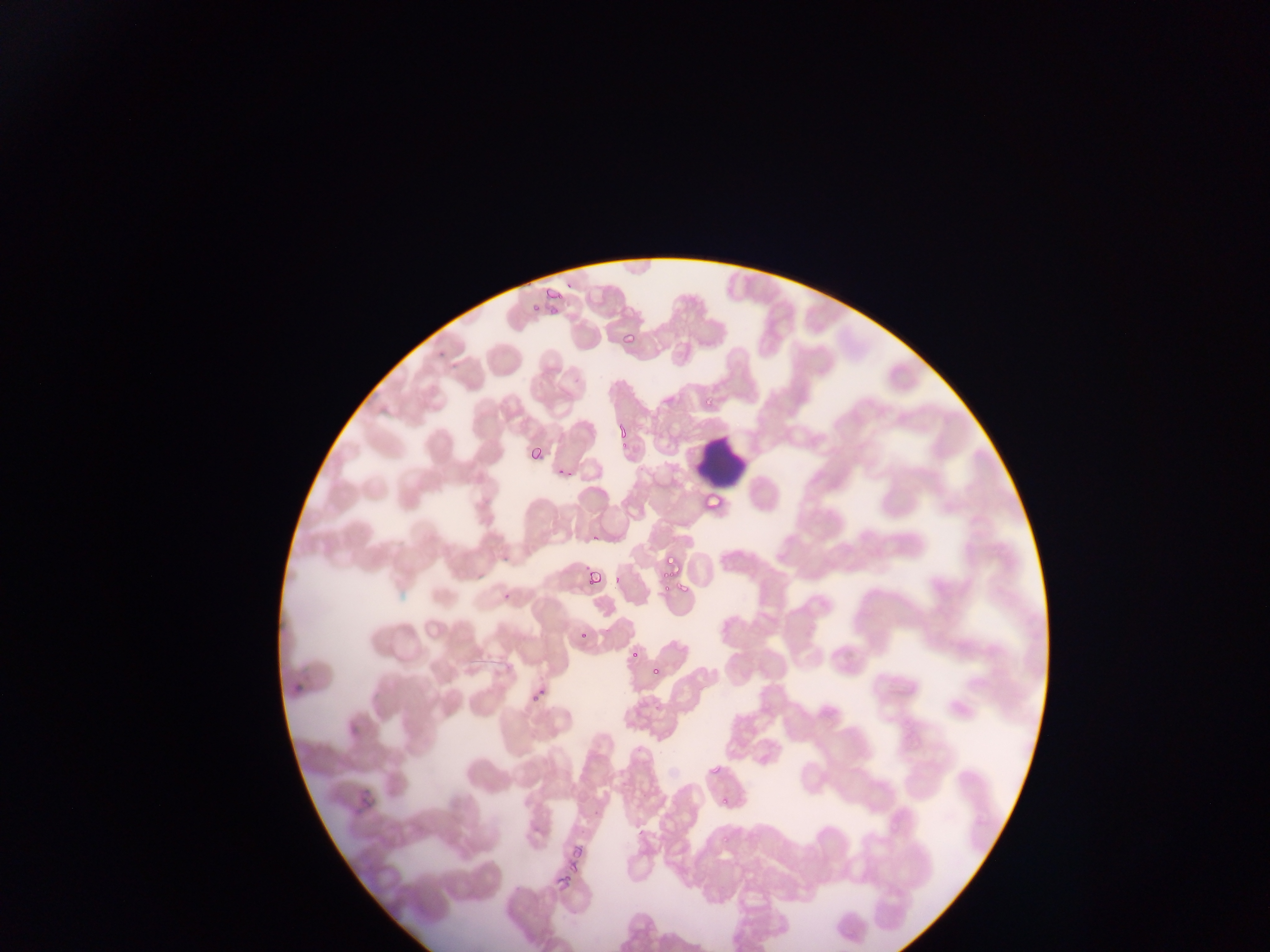

Approximate bounding boxes as {left, top, right, bottom} in pixels. Malaria parasite locations: {544, 283, 562, 315}, {528, 302, 539, 314}, {618, 330, 637, 345}, {701, 400, 715, 407}, {617, 419, 631, 438}, {528, 441, 546, 457}, {704, 494, 722, 510}, {662, 552, 679, 577}, {587, 568, 602, 586}, {662, 581, 672, 591}, {674, 581, 690, 592}, {578, 630, 593, 642}, {627, 649, 641, 660}, {650, 663, 662, 679}, {707, 757, 721, 776}, {717, 795, 731, 813}, {567, 839, 593, 865}, {554, 864, 578, 893}. Leukocyte locations: {694, 436, 747, 488}. Sample from Ghana. Thin blood film. Image is 1270×952 pixels. Single field of view. Photographed through a microscope with a mobile-phone camera.